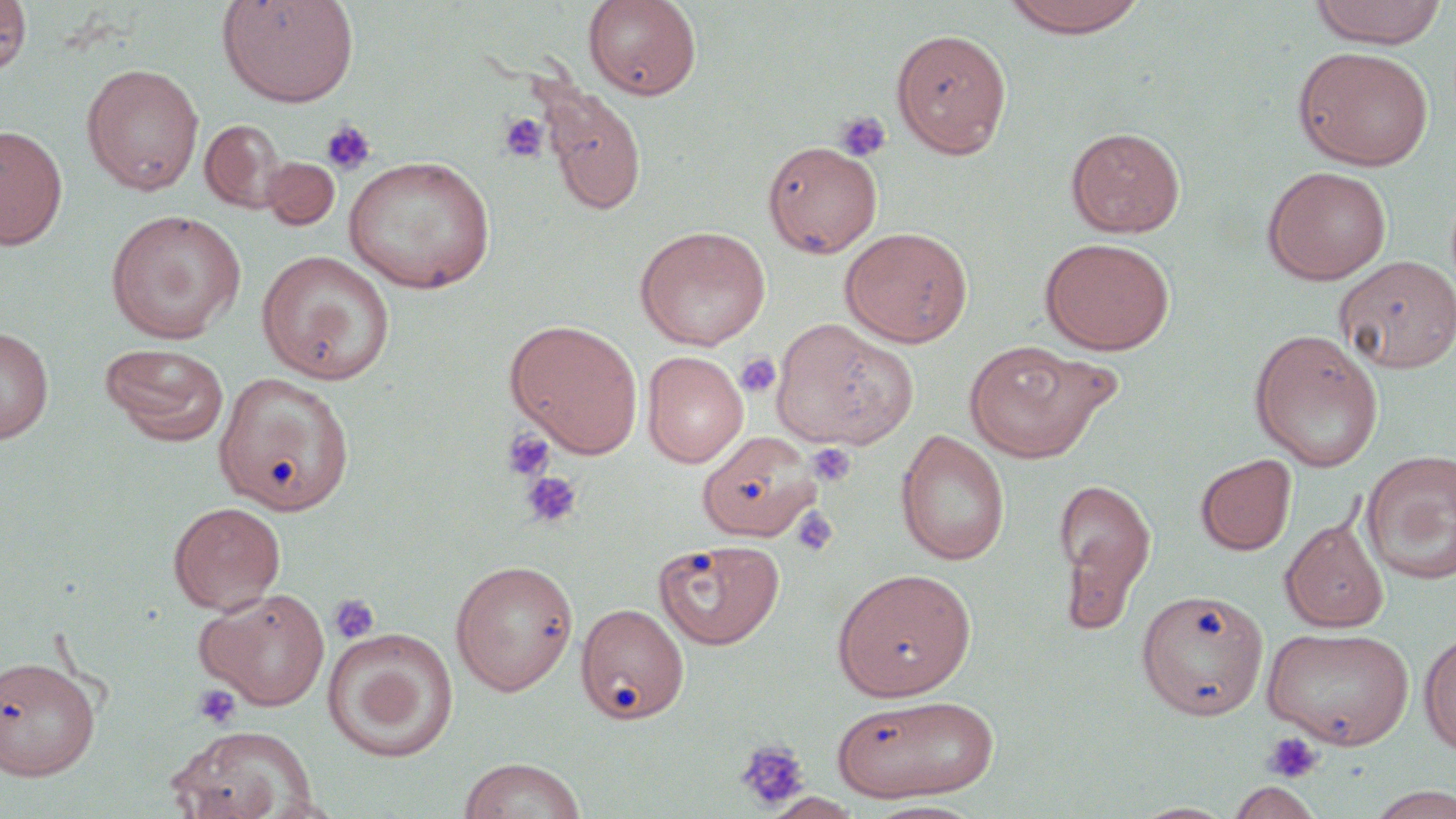

Approximate bounding boxes as (x1, y1, x2, y2) in pixels. Uninfected red blood cell locations: (0, 0, 32, 75), (217, 0, 359, 107), (583, 0, 702, 100), (998, 0, 1153, 38), (1309, 0, 1447, 48), (891, 27, 1012, 158), (1294, 46, 1434, 170), (81, 63, 204, 195), (540, 86, 647, 216), (200, 119, 290, 213), (0, 124, 68, 249), (1066, 126, 1186, 237), (762, 140, 883, 257), (343, 155, 496, 294), (260, 157, 340, 230), (1262, 165, 1392, 285), (106, 209, 247, 344), (635, 226, 771, 350), (839, 226, 973, 347), (1040, 237, 1175, 355), (257, 249, 395, 385), (1333, 255, 1456, 373), (505, 318, 643, 457), (770, 318, 918, 451), (0, 326, 54, 445), (1247, 327, 1384, 471), (964, 339, 1114, 463), (101, 343, 229, 446), (642, 350, 748, 468), (214, 371, 356, 516), (698, 430, 821, 541), (895, 430, 1011, 566), (1360, 450, 1456, 585), (1195, 454, 1297, 555), (1053, 476, 1157, 623), (168, 501, 286, 614), (1280, 518, 1389, 633), (654, 538, 784, 649), (450, 559, 579, 696), (832, 567, 976, 701), (196, 587, 331, 710), (1137, 588, 1269, 720), (576, 602, 690, 725), (1262, 626, 1415, 748), (324, 628, 458, 762), (1418, 629, 1456, 755), (1, 654, 102, 780), (830, 694, 1000, 802), (169, 726, 318, 819), (458, 757, 586, 819), (1225, 780, 1323, 819), (1362, 784, 1456, 819), (761, 792, 864, 818), (864, 799, 986, 818). Platelet locations: (833, 111, 891, 162), (498, 112, 549, 162), (321, 120, 376, 177), (735, 352, 781, 398), (501, 428, 556, 482), (808, 443, 856, 487), (521, 471, 583, 529), (791, 507, 839, 556), (329, 593, 380, 644), (192, 683, 242, 730), (1261, 730, 1324, 784), (734, 739, 810, 812). Slide-level diagnosis: no evidence of blood parasites. Thin blood smear. Single field of view. Image is 1456×819 pixels. Captured at 1000x magnification. May-Grünwald-Giemsa-stained preparation. Optical microscopy.